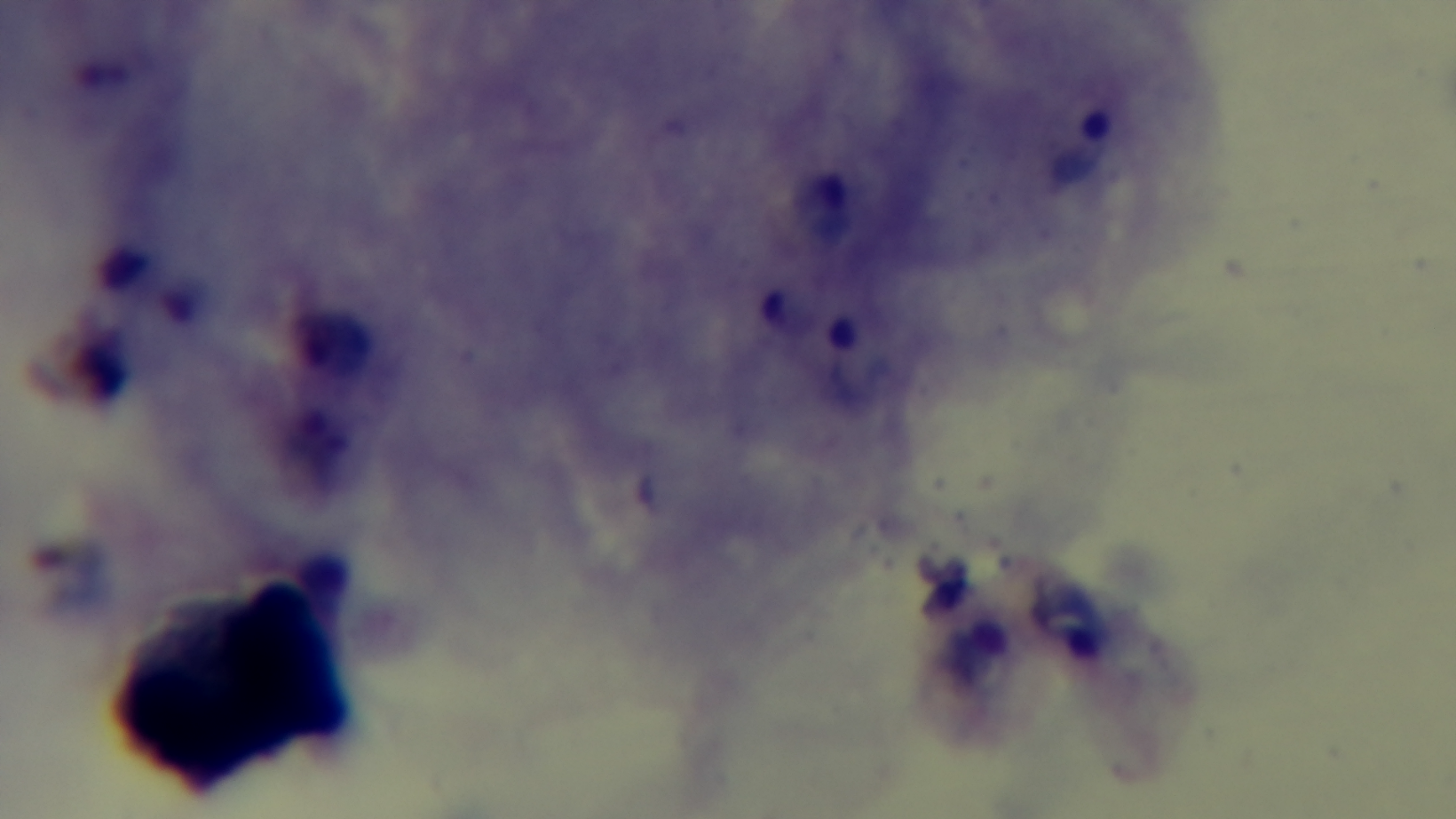

Summary:
  - Objective: 100x oil immersion
  - Capture: mounted 4K digital camera
  - Stain: Giemsa
  - Modality: light microscopy
  - Field of view: single
  - Preparation: thick
  - Malaria status: infected